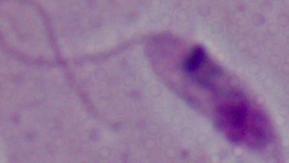
Summary:
  - Modality: photomicrograph
  - Magnification: 1000x
  - Identification: Leishmania